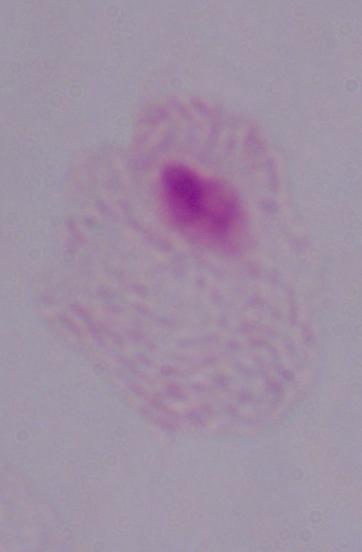

identification = trichomonad
modality = micrograph
magnification = 1000x